Report the malaria status of this cell.
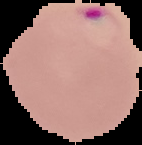
Parasitized.

The area outside the segmented cell region is set to black. Image is 142×145 pixels. From a thin blood smear.